Classify this cell by malaria status.
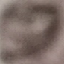

It is uninfected.

{
  "image_type": "automatically extracted cell patch, resized to 64 × 64 pixels",
  "stain": "Giemsa",
  "capture": "smartphone through the microscope eyepiece",
  "preparation": "thin smear"
}